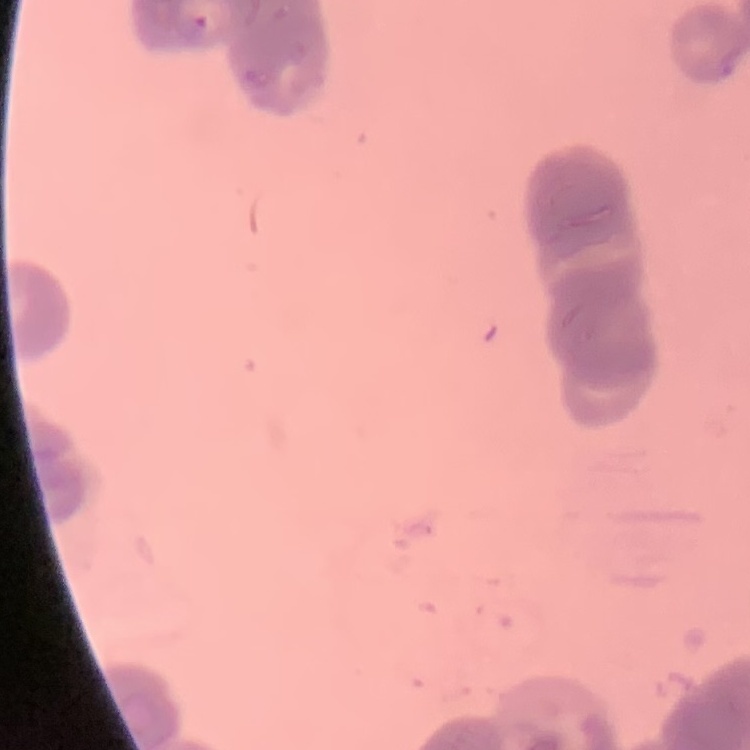
red_blood_cell_morphology: rouleaux formation
stain: Field's or Giemsa
image_type: one tile cut from a larger photomicrograph
preparation: thin peripheral smear